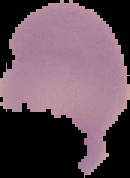
image type = segmented cell region with the area outside set to black
preparation = thin blood smear
image size = 130×178 pixels
result = no malaria parasites detected